Report the malaria status of this cell.
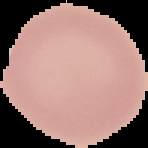
It is uninfected.

From a thin blood film. The area outside the segmented cell region is set to black. Image is 148×148 pixels.